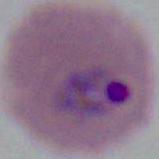 A Plasmodium parasite is shown. Micrograph. Captured at either 400x or 1000x magnification.